Give the extent of the malaria parasites you find, grouped by life-cycle stage — ring form, trophozoite, schizont, or gametocyte.
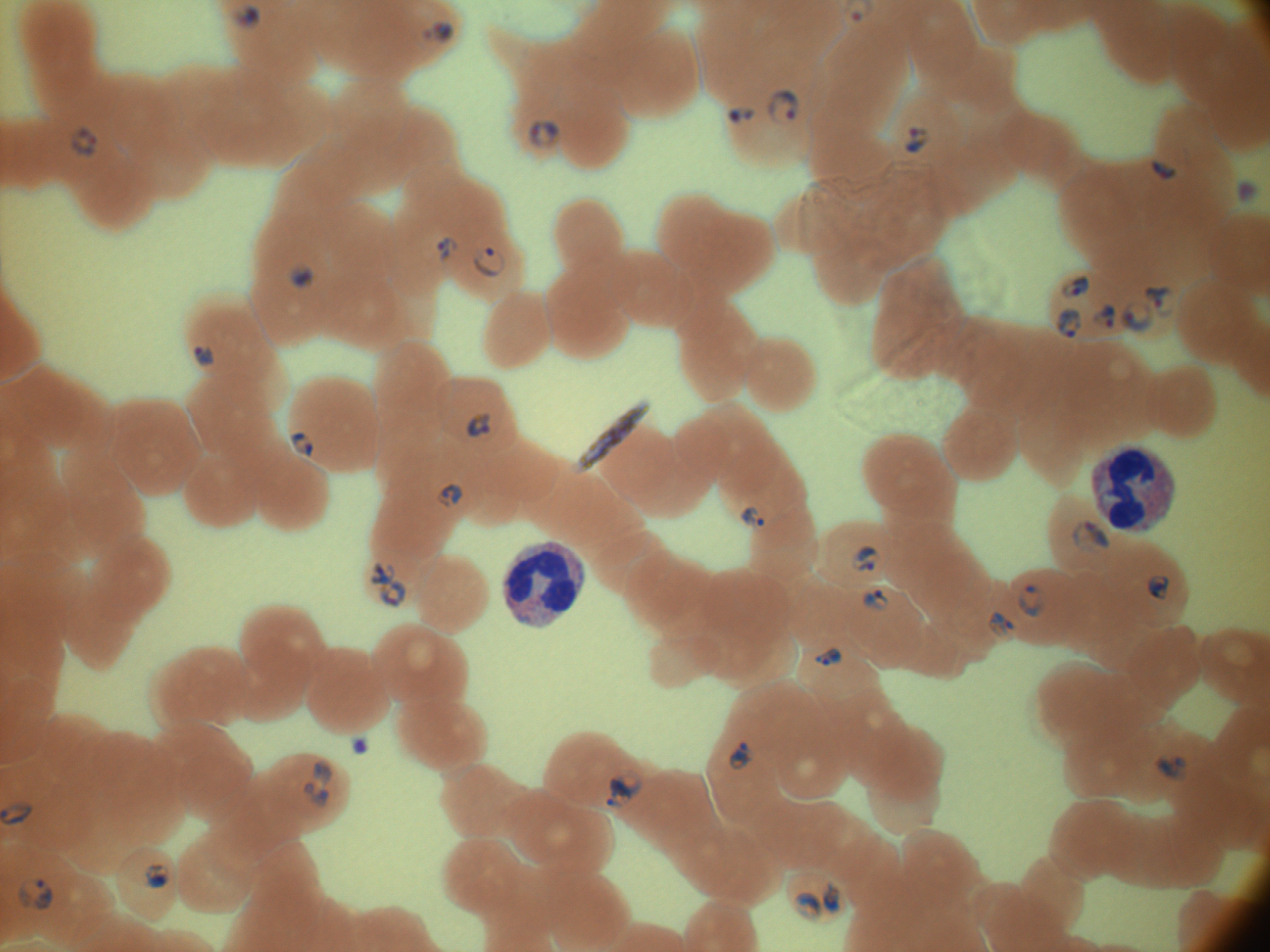
Approximate bounding boxes as named x1/y1/x2/y2 corners in pixels, from the source annotation, which is not necessarily exhaustive.
Ring forms: (x1=232, y1=4, x2=261, y2=29), (x1=420, y1=20, x2=456, y2=45), (x1=766, y1=89, x2=800, y2=124), (x1=728, y1=106, x2=756, y2=123), (x1=527, y1=118, x2=562, y2=150), (x1=71, y1=125, x2=98, y2=159), (x1=903, y1=126, x2=932, y2=154), (x1=1150, y1=160, x2=1178, y2=180), (x1=1237, y1=181, x2=1259, y2=203), (x1=437, y1=236, x2=459, y2=262), (x1=472, y1=246, x2=505, y2=277), (x1=288, y1=260, x2=315, y2=290), (x1=1060, y1=273, x2=1091, y2=299), (x1=1144, y1=285, x2=1175, y2=317), (x1=1120, y1=300, x2=1156, y2=334), (x1=1091, y1=302, x2=1117, y2=332), (x1=1055, y1=307, x2=1082, y2=338), (x1=194, y1=345, x2=215, y2=366), (x1=466, y1=411, x2=492, y2=439), (x1=288, y1=430, x2=314, y2=458), (x1=437, y1=483, x2=464, y2=508), (x1=740, y1=506, x2=766, y2=530), (x1=1071, y1=518, x2=1111, y2=555), (x1=849, y1=545, x2=882, y2=572), (x1=369, y1=561, x2=396, y2=589), (x1=1147, y1=574, x2=1170, y2=601), (x1=377, y1=579, x2=407, y2=609), (x1=1017, y1=582, x2=1048, y2=618), (x1=861, y1=588, x2=890, y2=612), (x1=985, y1=610, x2=1016, y2=639), (x1=814, y1=648, x2=842, y2=666), (x1=728, y1=739, x2=756, y2=771), (x1=1154, y1=753, x2=1188, y2=783), (x1=310, y1=759, x2=334, y2=785), (x1=606, y1=768, x2=641, y2=808), (x1=301, y1=781, x2=329, y2=808), (x1=144, y1=863, x2=171, y2=889), (x1=17, y1=878, x2=54, y2=910), (x1=822, y1=879, x2=842, y2=914), (x1=793, y1=891, x2=824, y2=920).
Gametocytes: (x1=579, y1=399, x2=651, y2=472).

Life-cycle stages among the annotated parasites: ring form, gametocyte. Thin blood smear. Species: Plasmodium falciparum. Captured at 100x magnification. Image is 1270×952 pixels. Giemsa-stained preparation. One field from this slide. Leica DM2000 optical microscope with a built-in camera.